Assess this cell for malaria.
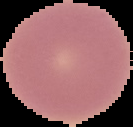

Uninfected.

image_size: 133×127 pixels
image_type: segmented cell region on a black background
preparation: thin blood film